Report the malaria status.
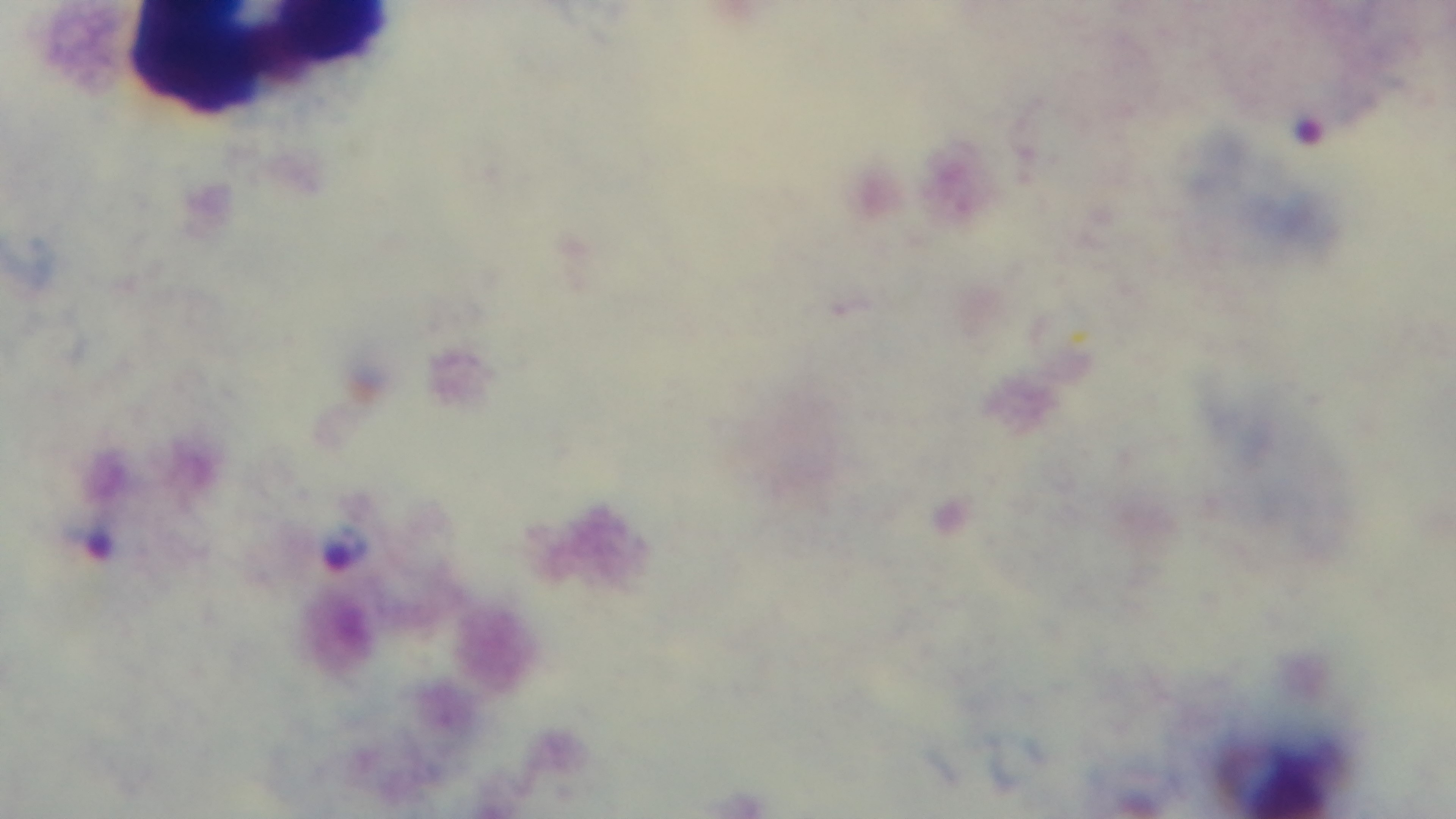
Infected.

Captured with a mounted 4K digital camera. Preparation: thick. Oil-immersion objective, 100x. One field from the slide. Giemsa stain. Light microscopy.